Classify this cell by malaria status.
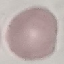

Uninfected.

Summary:
  - Stain: Giemsa
  - Preparation: thin blood film
  - Image type: cell patch, automatically extracted from a larger field of view and resized to 64 × 64 pixels
  - Capture: smartphone through the microscope eyepiece